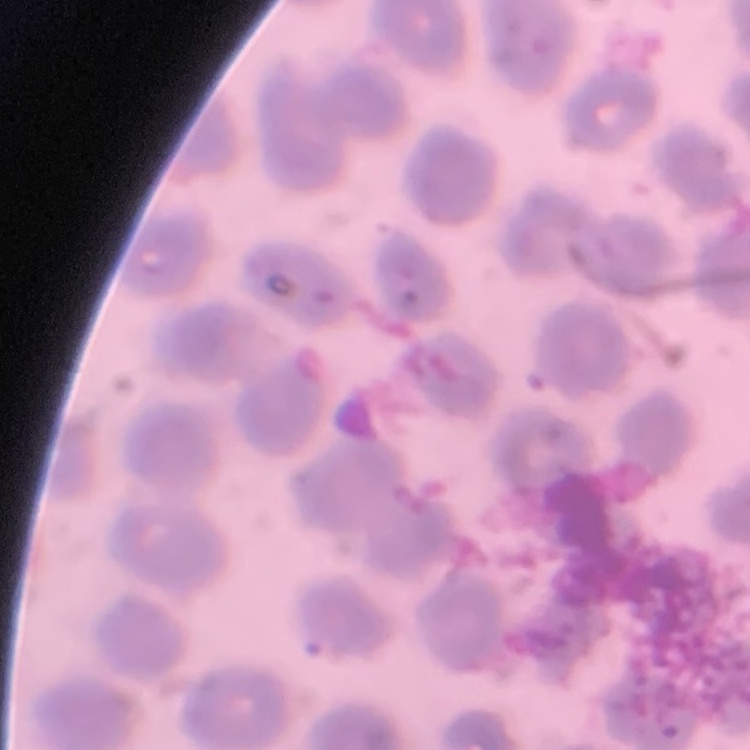

red_blood_cell_morphology: no rouleaux formation
image_type: one tile cut from a larger photomicrograph
preparation: thin blood film
stain: Field's or Giemsa